Assess this cell for malaria.
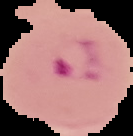
Parasitized.

image type = cell region segmented out of the field of view; surrounding area masked to black
image size = 133×136 pixels
preparation = thin blood film